Locate every uninfected red blood cell.
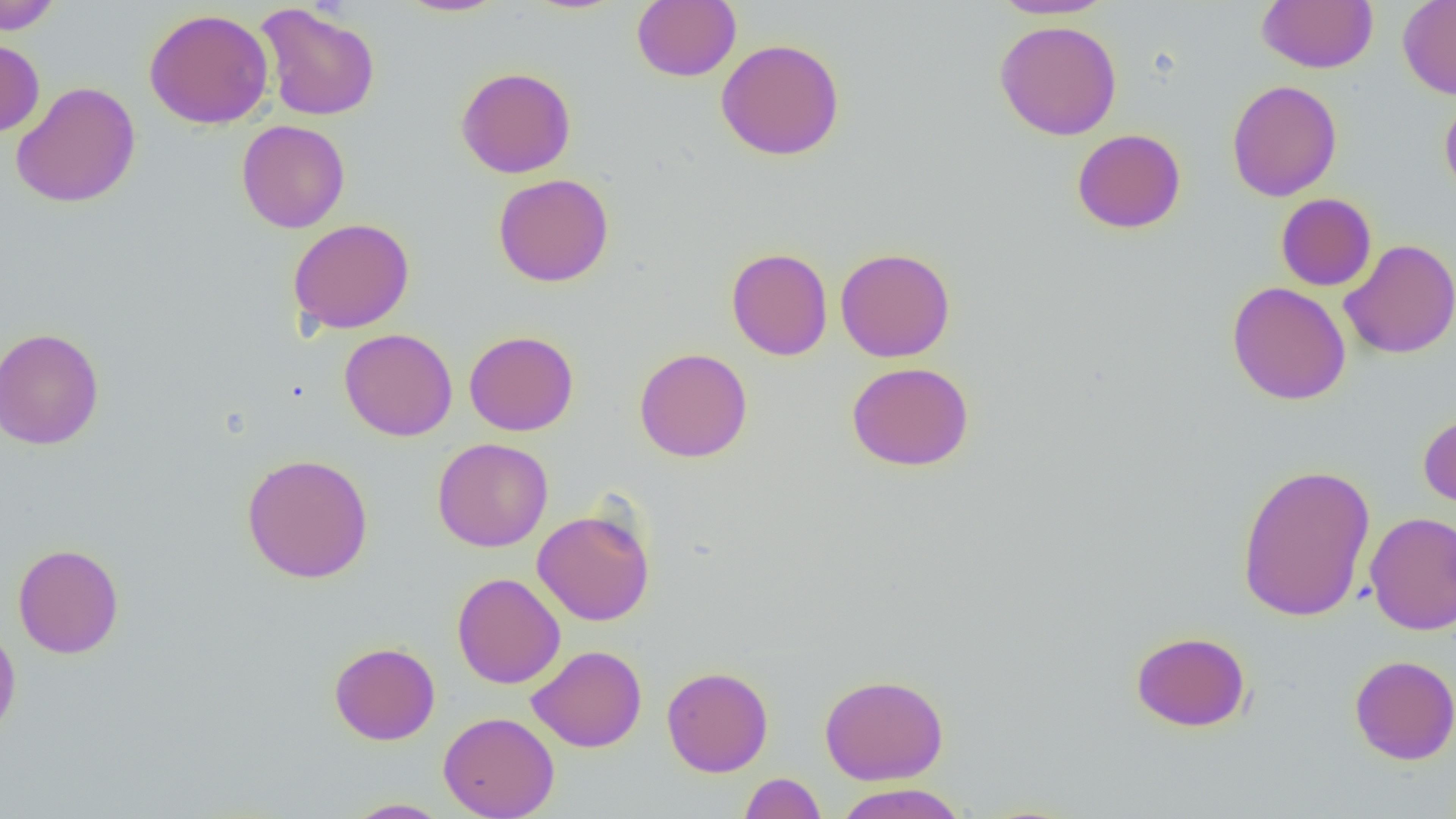
Approximate bounding boxes as named x1/y1/x2/y2 corners in pixels.
Uninfected red blood cells: (x1=0, y1=0, x2=62, y2=35), (x1=397, y1=0, x2=508, y2=17), (x1=990, y1=0, x2=1115, y2=20), (x1=1256, y1=0, x2=1378, y2=74), (x1=632, y1=1, x2=741, y2=81), (x1=1398, y1=1, x2=1456, y2=100), (x1=256, y1=3, x2=381, y2=121), (x1=144, y1=8, x2=274, y2=129), (x1=994, y1=20, x2=1122, y2=141), (x1=0, y1=37, x2=45, y2=137), (x1=716, y1=38, x2=845, y2=160), (x1=456, y1=66, x2=576, y2=178), (x1=1226, y1=79, x2=1343, y2=202), (x1=10, y1=82, x2=141, y2=208), (x1=1440, y1=92, x2=1456, y2=202), (x1=236, y1=119, x2=350, y2=233), (x1=1072, y1=129, x2=1186, y2=234), (x1=493, y1=173, x2=614, y2=287), (x1=1276, y1=193, x2=1377, y2=291), (x1=287, y1=218, x2=415, y2=334), (x1=1339, y1=239, x2=1456, y2=359), (x1=726, y1=247, x2=833, y2=361), (x1=835, y1=247, x2=955, y2=362), (x1=1226, y1=281, x2=1351, y2=405), (x1=1, y1=327, x2=104, y2=450), (x1=340, y1=328, x2=457, y2=441), (x1=464, y1=331, x2=579, y2=436), (x1=634, y1=348, x2=752, y2=463), (x1=846, y1=361, x2=974, y2=471), (x1=1418, y1=410, x2=1456, y2=512), (x1=432, y1=438, x2=553, y2=552), (x1=241, y1=453, x2=373, y2=583), (x1=1237, y1=463, x2=1376, y2=622), (x1=532, y1=507, x2=656, y2=626), (x1=1365, y1=512, x2=1456, y2=635), (x1=13, y1=543, x2=124, y2=659), (x1=451, y1=572, x2=565, y2=689), (x1=0, y1=623, x2=21, y2=744), (x1=1130, y1=630, x2=1251, y2=732), (x1=329, y1=642, x2=440, y2=745), (x1=527, y1=645, x2=647, y2=752), (x1=1349, y1=655, x2=1456, y2=765), (x1=661, y1=666, x2=773, y2=777), (x1=819, y1=673, x2=949, y2=785), (x1=438, y1=711, x2=560, y2=819), (x1=739, y1=772, x2=826, y2=819), (x1=833, y1=783, x2=969, y2=819), (x1=344, y1=798, x2=451, y2=818).

{
  "slide_level_diagnosis": "negative for blood parasites",
  "magnification": "1000x",
  "field_of_view": "single",
  "modality": "optical microscopy",
  "image_size": "1456×819 pixels",
  "preparation": "thin blood smear"
}